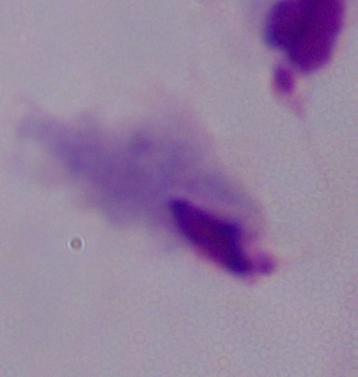

A trichomonad is seen. Micrograph. Captured at 1000x magnification.